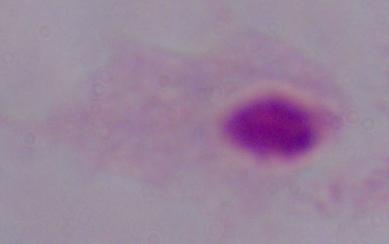

Summary:
  - Identification: trichomonad
  - Modality: photomicrograph
  - Magnification: 1000x